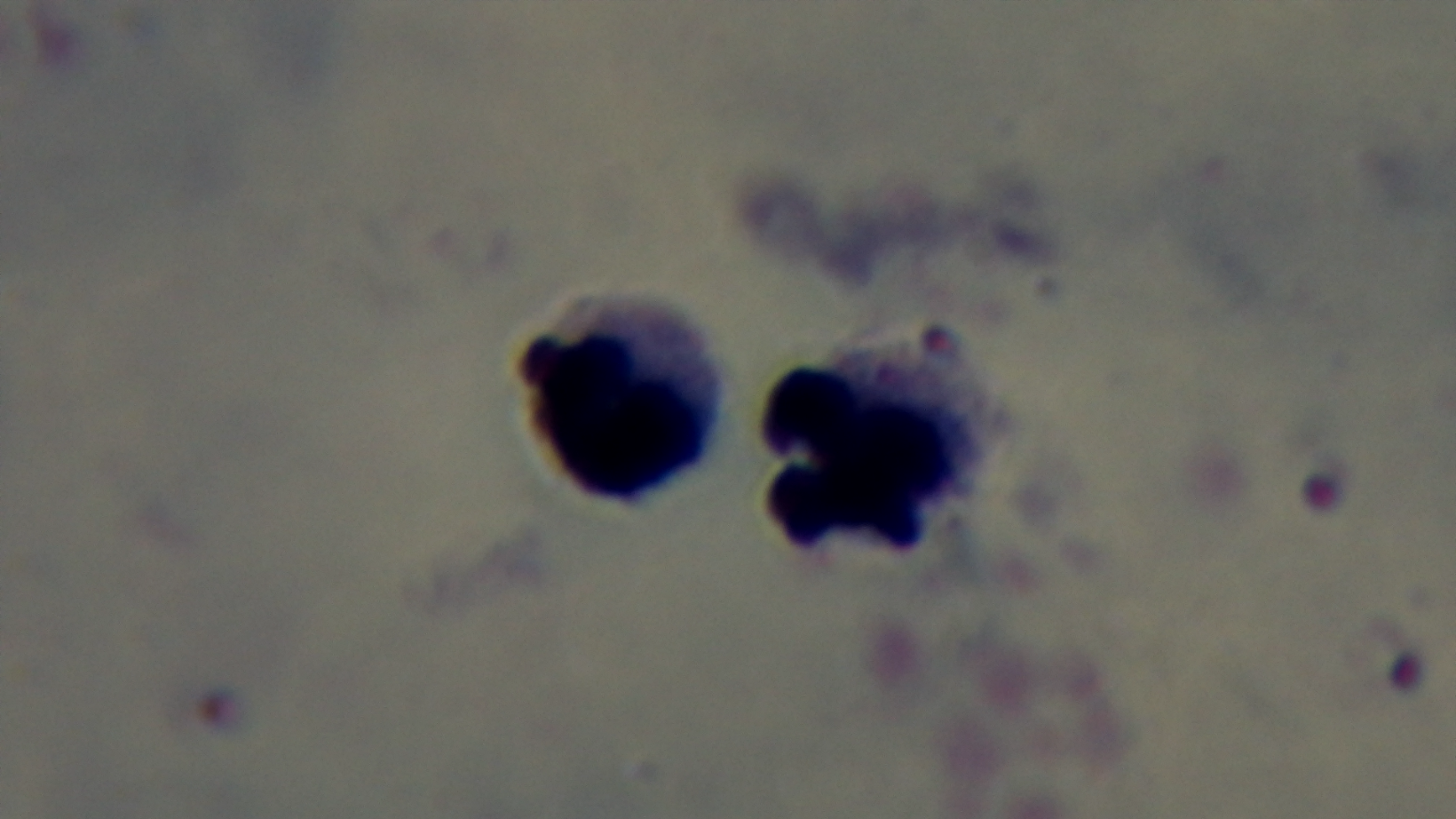
preparation: thick smear
modality: light microscopy
capture: mounted 4K digital camera
objective: 100x oil immersion
field_of_view: single
stain: Giemsa
malaria_status: positive